Name the parasite shown.
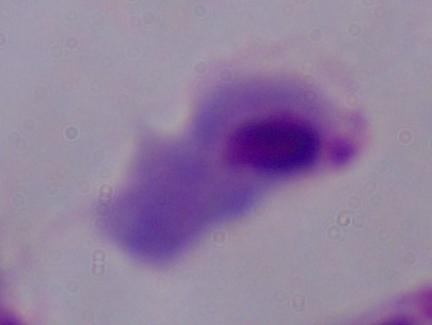

This is a trichomonad.

Summary:
  - Magnification: 1000x
  - Modality: photomicrograph